Assess this cell for malaria.
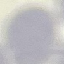
Uninfected.

Thin blood smear. Automatically extracted cell patch, resized to 64 × 64 pixels. Photographed with a smartphone camera at the microscope eyepiece. Giemsa stain.